Assess the morphology of the erythrocytes.
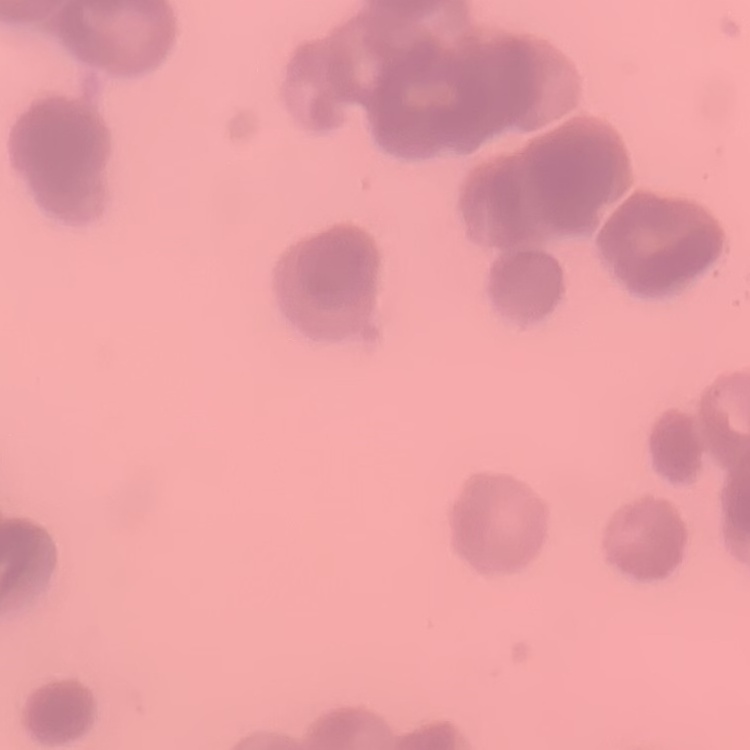
Rouleaux formation.

One tile cut from a larger photomicrograph. Field's or Giemsa stain. Thin peripheral smear.